Classify this cell by malaria status.
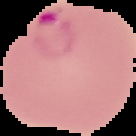
It is parasitized.

Summary:
  - Image size: 136×136 pixels
  - Image type: segmented cell region with the area outside set to black
  - Preparation: thin blood film